Assess the morphology of the erythrocytes.
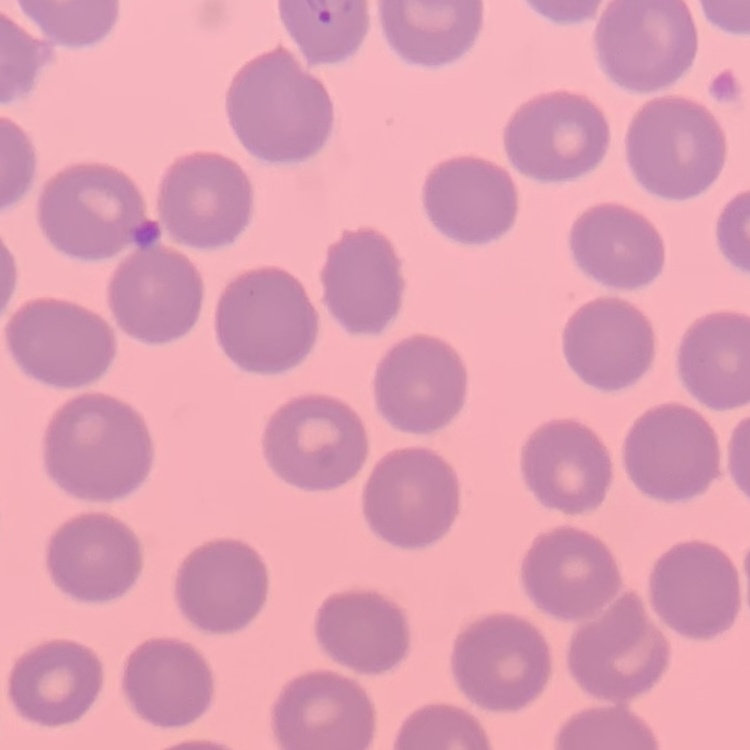

They show no rouleaux formation.

Summary:
  - Stain: Field's or Giemsa
  - Image type: one tile cut from a larger photomicrograph
  - Preparation: thin blood smear